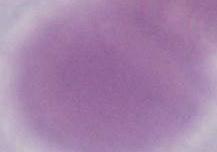
identification = erythrocyte
modality = micrograph
magnification = 1000x